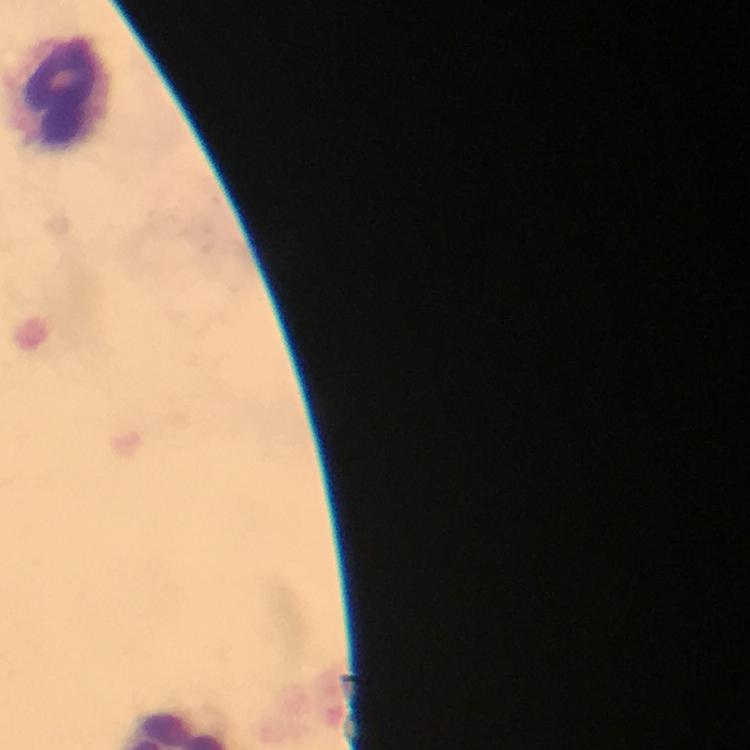
Approximate centers as (x, y) in pixels.
Summary:
  - Leukocyte locations: (63, 91)
  - Magnification: 100x
  - Preparation: thick blood film
  - Context: from a malaria diagnostic workup
  - Capture: smartphone photograph through a microscope
  - Immersion oil: applied
  - Malaria parasites: none seen
  - Image size: 750×750 pixels
  - Cropped from: one field of view
  - Stain: Giemsa